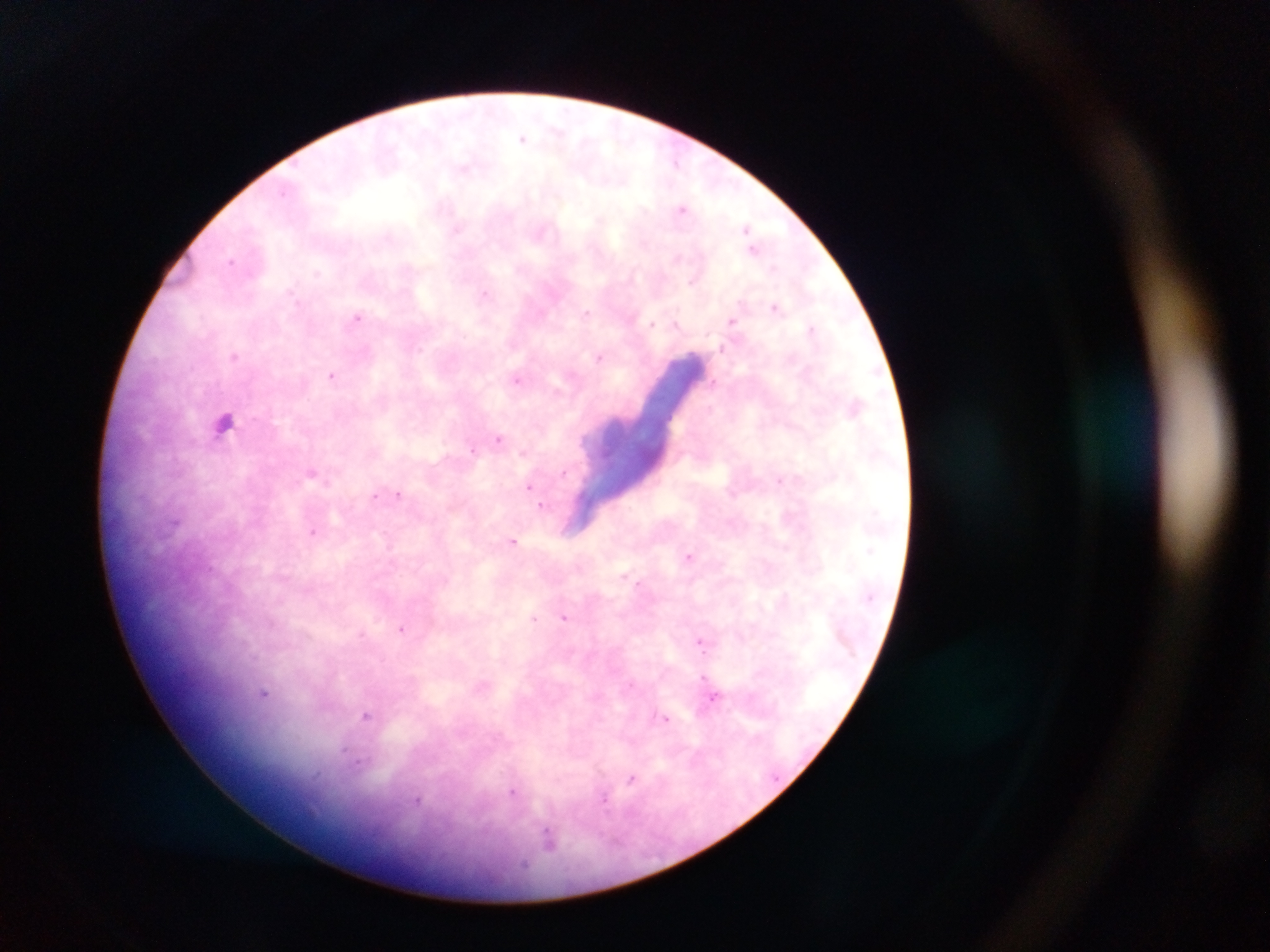
Approximate centers as [x, y] in pixels.
Summary:
  - Leukocyte locations: [225, 423]
  - Malaria parasite locations: [524, 138], [675, 160], [462, 170], [283, 193], [682, 207], [443, 208], [746, 227], [754, 248], [231, 259], [318, 273], [485, 293], [775, 306], [585, 311], [357, 316], [733, 320], [652, 321], [811, 328], [418, 348], [599, 355], [234, 357], [331, 377], [517, 380], [499, 438], [472, 448], [522, 452], [780, 479], [528, 487], [399, 495], [376, 496], [543, 505], [176, 522], [514, 543], [869, 551], [691, 555], [564, 617], [535, 619], [402, 627], [700, 641], [702, 649], [703, 678], [263, 695], [717, 695], [367, 717], [664, 719], [344, 751], [631, 780], [515, 790], [606, 800], [419, 801], [312, 812], [548, 836]
  - Field of view: single
  - Preparation: thick blood smear
  - Capture: mobile-phone photograph through a microscope
  - Image size: 1270×952 pixels
  - Country: Ghana